Outline each Plasmodium malariae-infected red blood cell.
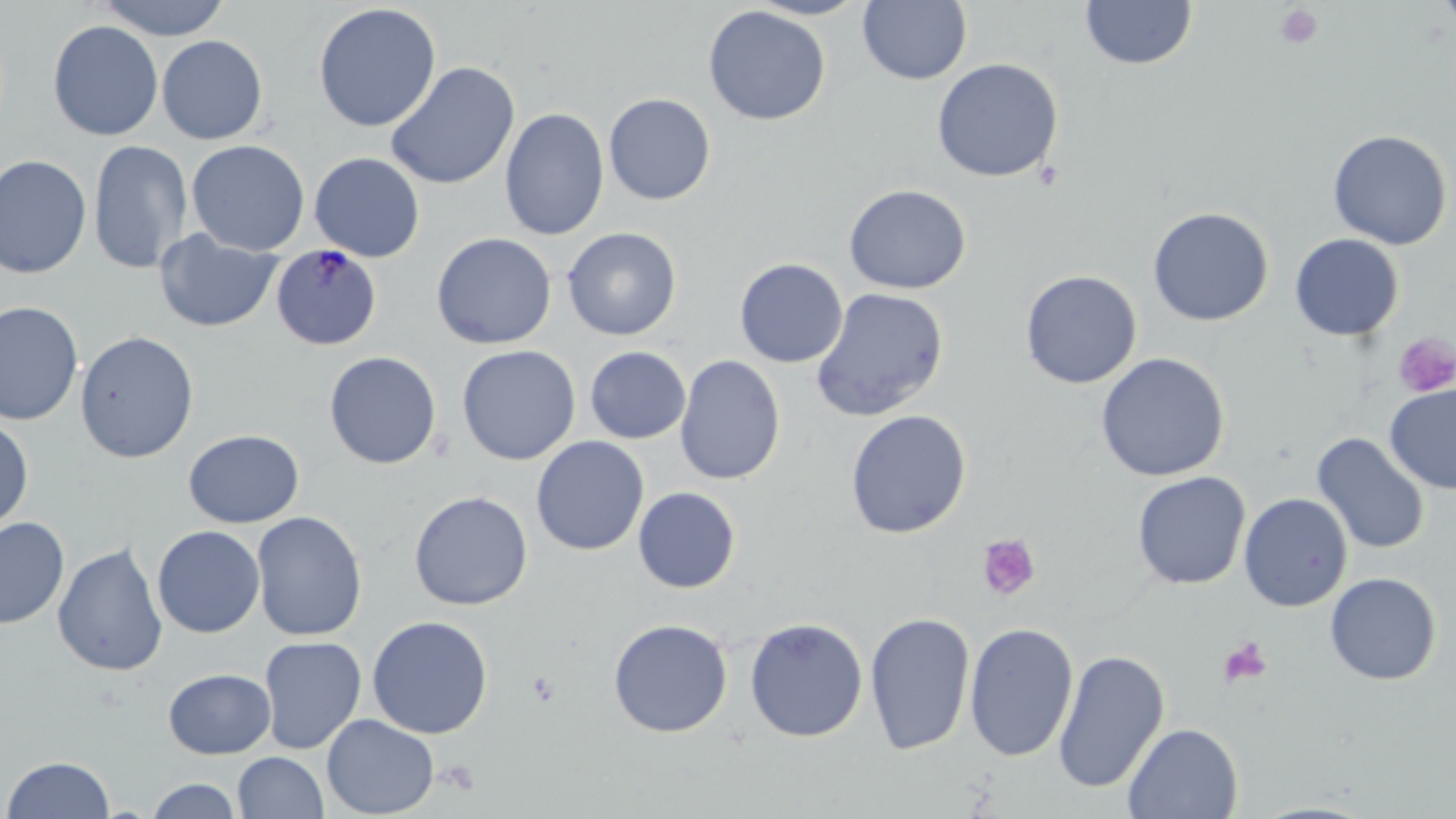
Approximate bounding boxes as (x1,y1)-(x2,y2) corner pairs in pixels.
Plasmodium malariae-infected red blood cells: (270,243)-(382,351).

slide-level diagnosis = Plasmodium malariae
preparation = thin blood film
stain = May-Grünwald-Giemsa
field of view = one of a larger specimen
magnification = 1000x
modality = light microscopy
image size = 1456×819 pixels
uninfected red blood cell locations = approximate bounding boxes as (x1,y1)-(x2,y2) corner pairs in pixels: (95,0)-(233,40), (745,0)-(870,21), (1079,0)-(1198,71), (1435,0)-(1456,30), (857,1)-(973,85), (312,3)-(441,132), (703,5)-(830,126), (47,19)-(163,141), (156,35)-(268,144), (931,58)-(1064,183), (385,61)-(520,190), (603,93)-(716,205), (499,107)-(609,241), (1327,129)-(1453,250), (87,139)-(193,275), (186,139)-(310,256), (309,152)-(426,262), (0,154)-(93,279), (843,183)-(971,295), (1147,206)-(1274,326), (562,227)-(682,341), (153,229)-(283,333), (431,232)-(557,350), (1289,233)-(1404,341), (734,258)-(848,368), (1019,270)-(1142,389), (810,287)-(949,422), (0,300)-(84,426), (74,331)-(200,464), (456,345)-(581,465), (585,346)-(691,444), (323,351)-(442,469), (1095,352)-(1231,482), (675,354)-(785,485), (1384,384)-(1456,494), (845,409)-(972,539), (0,415)-(34,534), (183,429)-(305,528), (1311,433)-(1430,555), (531,436)-(649,556), (1131,471)-(1251,590), (633,487)-(741,593), (408,490)-(533,610), (1238,492)-(1353,612), (251,511)-(368,641), (0,517)-(70,630), (152,525)-(265,638), (52,541)-(169,677), (1324,572)-(1442,685), (864,611)-(976,756), (367,615)-(494,739), (744,617)-(868,742), (608,618)-(733,738), (964,621)-(1079,762), (258,636)-(367,754), (1052,648)-(1170,794), (162,668)-(276,759), (321,714)-(439,818), (1122,722)-(1244,818), (233,751)-(329,818), (2,754)-(116,818), (144,777)-(242,818)
platelet locations = approximate bounding boxes as (x1,y1)-(x2,y2) corner pairs in pixels: (1274,4)-(1324,49), (1392,333)-(1455,398), (977,534)-(1041,601), (1218,637)-(1272,688)